Assess the morphology of the erythrocytes.
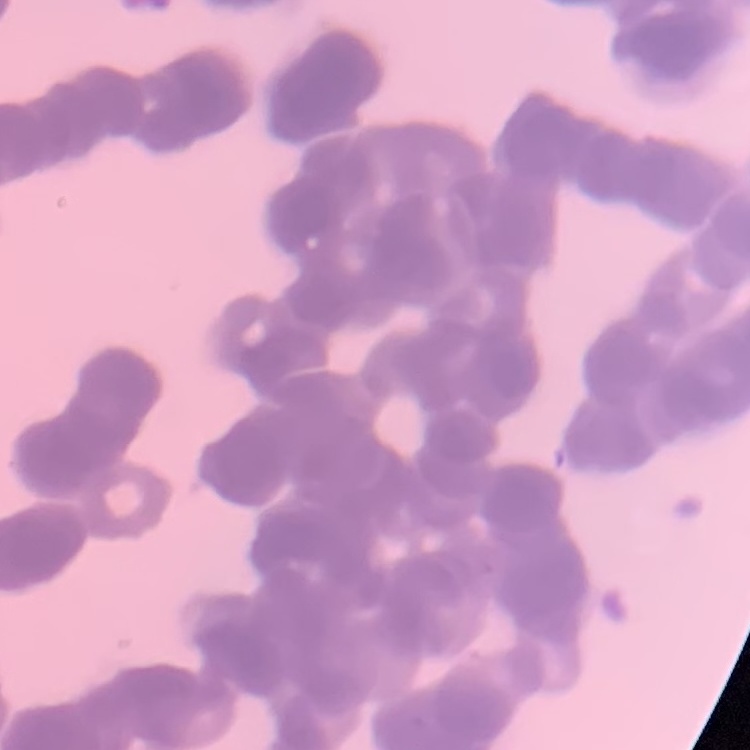
Rouleaux formation.

image type = one tile cut from a larger photomicrograph
preparation = thin peripheral smear
stain = Field's or Giemsa